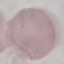
Summary:
  - Malaria status: uninfected
  - Image type: automatically extracted cell patch, resized to 64 × 64 pixels
  - Stain: Giemsa
  - Preparation: thin smear
  - Capture: smartphone through the microscope eyepiece